Describe the morphology of the erythrocytes.
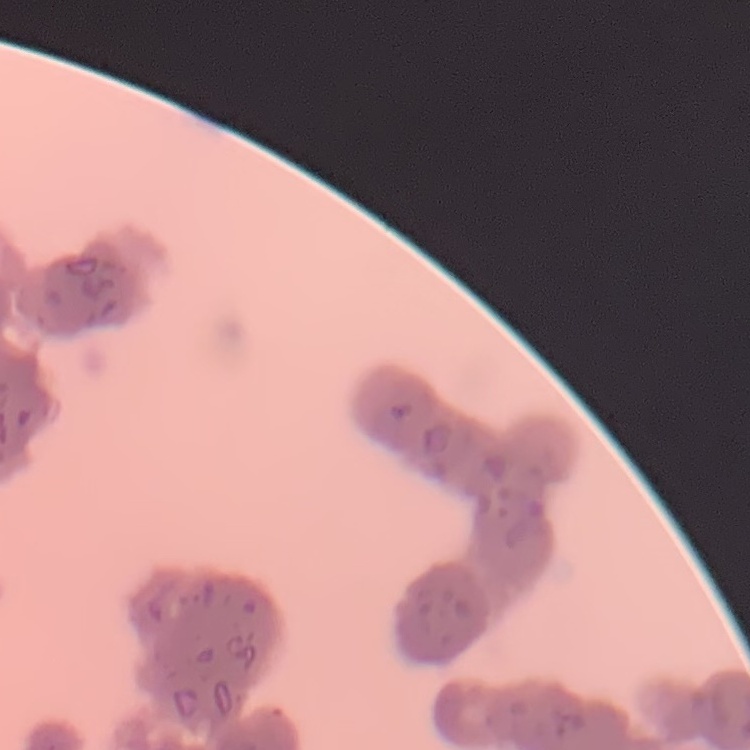
Rouleaux formation.

stain = Field's or Giemsa
preparation = thin blood film
image type = square crop of a larger photomicrograph